Report the malaria status of this cell.
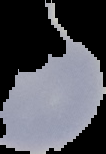

Uninfected.

From a thin blood film. Image is 106×154 pixels. The area outside the segmented cell region is set to black.